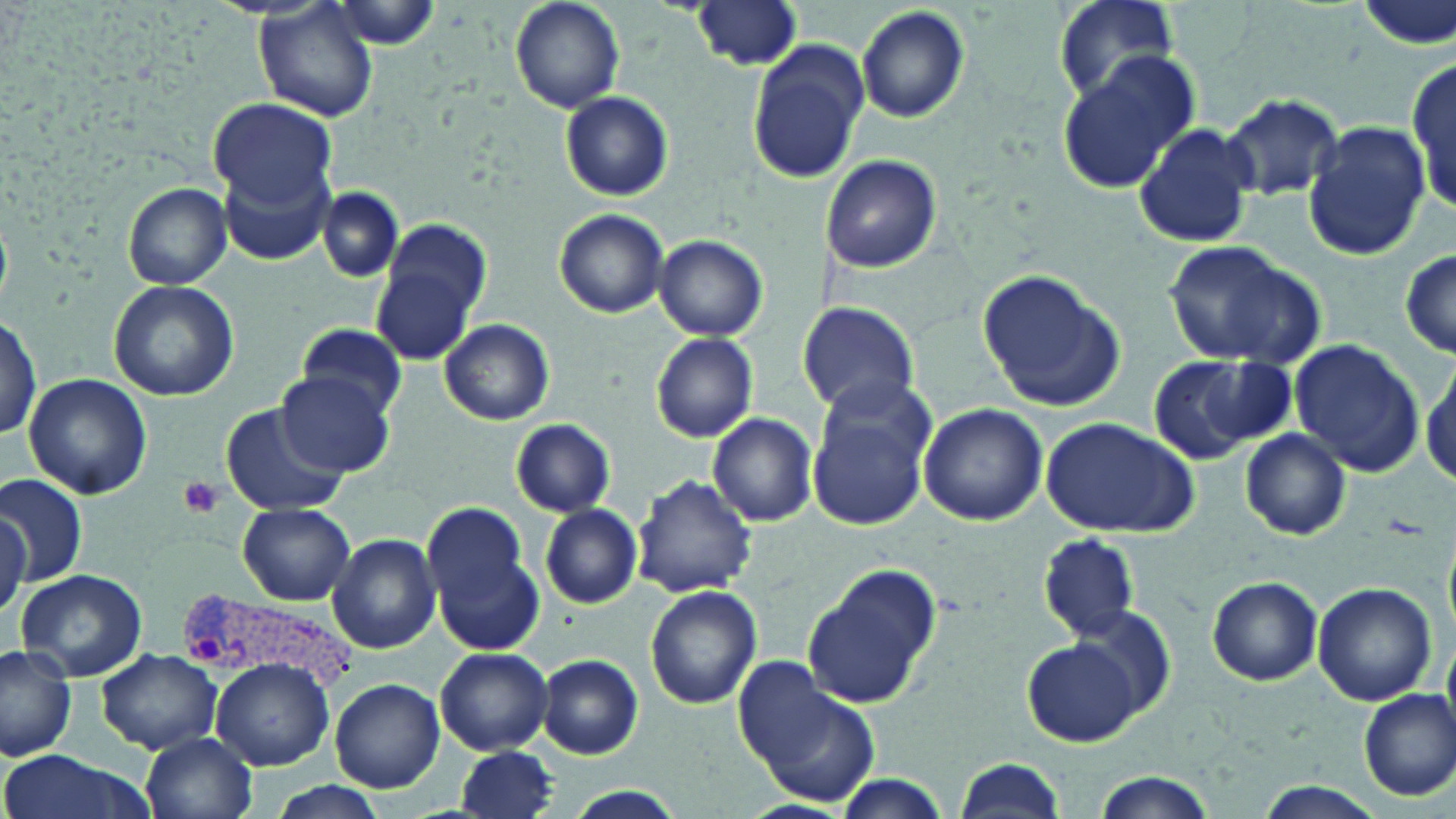
Approximate bounding boxes as named x1/y1/x2/y2 corners in pixels. Platelet locations: (x1=176, y1=477, x2=226, y2=519). Uninfected red blood cell locations: (x1=254, y1=0, x2=381, y2=124), (x1=511, y1=0, x2=624, y2=114), (x1=1053, y1=0, x2=1179, y2=102), (x1=690, y1=1, x2=805, y2=71), (x1=330, y1=2, x2=442, y2=49), (x1=856, y1=5, x2=970, y2=123), (x1=746, y1=39, x2=870, y2=185), (x1=1410, y1=49, x2=1456, y2=217), (x1=1056, y1=54, x2=1197, y2=188), (x1=560, y1=91, x2=672, y2=201), (x1=1226, y1=92, x2=1345, y2=201), (x1=209, y1=98, x2=337, y2=210), (x1=1304, y1=122, x2=1428, y2=261), (x1=1131, y1=123, x2=1257, y2=248), (x1=821, y1=154, x2=941, y2=273), (x1=219, y1=157, x2=333, y2=265), (x1=123, y1=184, x2=229, y2=289), (x1=318, y1=187, x2=403, y2=281), (x1=555, y1=209, x2=667, y2=318), (x1=375, y1=218, x2=492, y2=358), (x1=654, y1=234, x2=770, y2=341), (x1=1163, y1=241, x2=1320, y2=367), (x1=1400, y1=251, x2=1456, y2=359), (x1=979, y1=268, x2=1126, y2=410), (x1=108, y1=280, x2=238, y2=402), (x1=797, y1=299, x2=921, y2=418), (x1=1, y1=315, x2=41, y2=445), (x1=440, y1=317, x2=555, y2=426), (x1=297, y1=323, x2=407, y2=418), (x1=650, y1=333, x2=758, y2=442), (x1=1289, y1=339, x2=1425, y2=475), (x1=1194, y1=353, x2=1300, y2=451), (x1=1418, y1=353, x2=1455, y2=491), (x1=1146, y1=357, x2=1258, y2=463), (x1=277, y1=371, x2=392, y2=476), (x1=23, y1=372, x2=150, y2=501), (x1=807, y1=389, x2=934, y2=529), (x1=223, y1=402, x2=345, y2=516), (x1=920, y1=403, x2=1047, y2=526), (x1=706, y1=413, x2=819, y2=527), (x1=1039, y1=416, x2=1200, y2=538), (x1=511, y1=419, x2=615, y2=517), (x1=1241, y1=429, x2=1352, y2=540), (x1=1, y1=473, x2=88, y2=583), (x1=633, y1=475, x2=757, y2=598), (x1=236, y1=503, x2=355, y2=605), (x1=423, y1=503, x2=527, y2=611), (x1=539, y1=503, x2=643, y2=609), (x1=0, y1=504, x2=31, y2=616), (x1=326, y1=533, x2=441, y2=653), (x1=430, y1=533, x2=546, y2=660), (x1=1039, y1=534, x2=1139, y2=640), (x1=803, y1=564, x2=939, y2=707), (x1=14, y1=569, x2=147, y2=682), (x1=1207, y1=576, x2=1322, y2=685), (x1=1313, y1=580, x2=1437, y2=705), (x1=644, y1=584, x2=760, y2=710), (x1=1064, y1=606, x2=1178, y2=726), (x1=1023, y1=638, x2=1142, y2=747), (x1=0, y1=644, x2=76, y2=760), (x1=435, y1=647, x2=554, y2=755), (x1=97, y1=649, x2=223, y2=753), (x1=537, y1=654, x2=644, y2=760), (x1=208, y1=657, x2=334, y2=769), (x1=733, y1=660, x2=880, y2=809), (x1=330, y1=679, x2=445, y2=792), (x1=1358, y1=689, x2=1456, y2=800), (x1=143, y1=731, x2=258, y2=819), (x1=458, y1=746, x2=559, y2=819), (x1=0, y1=750, x2=149, y2=819), (x1=953, y1=756, x2=1067, y2=819), (x1=1090, y1=773, x2=1220, y2=819), (x1=830, y1=774, x2=952, y2=818), (x1=263, y1=779, x2=388, y2=819), (x1=1258, y1=783, x2=1382, y2=817), (x1=558, y1=787, x2=691, y2=819). Plasmodium vivax-infected red blood cell locations: (x1=178, y1=590, x2=361, y2=695). Slide-level diagnosis: Plasmodium vivax. May-Grünwald-Giemsa stain. Optical microscopy. Image is 1456×819 pixels. Thin blood smear. Captured at 1000x magnification. Single field of view.